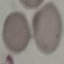

Summary:
  - Result: negative for malaria parasites
  - Image type: automatically extracted cell patch, resized to 64 × 64 pixels
  - Capture: smartphone camera at the microscope eyepiece
  - Stain: Giemsa
  - Preparation: thin smear